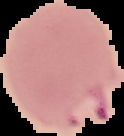
Summary:
  - Image type: cell region segmented out of the field of view; surrounding area masked to black
  - Result: Plasmodium parasites identified
  - Preparation: thin blood smear
  - Image size: 124×136 pixels